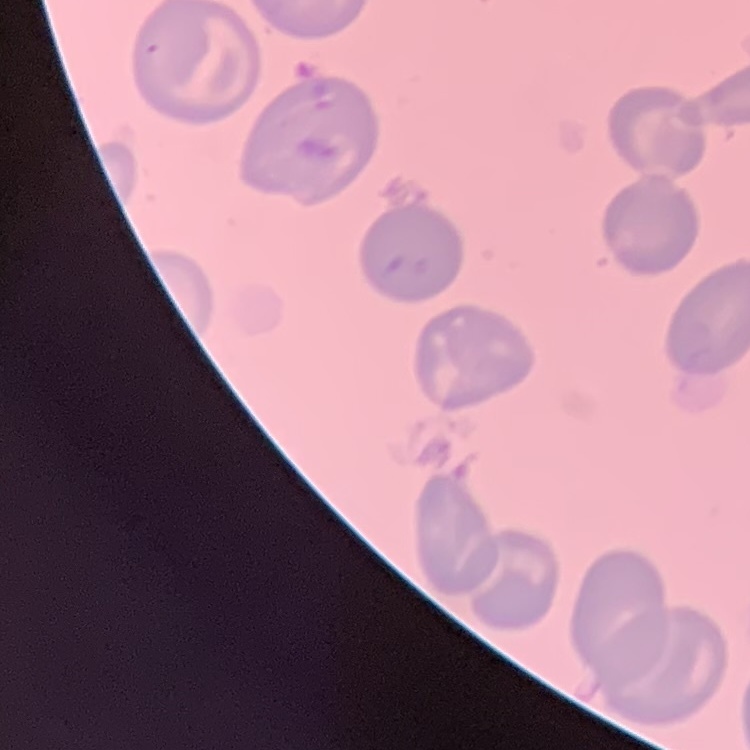

Summary:
  - Red blood cell morphology: no rouleaux formation
  - Image type: square crop of a larger photomicrograph
  - Stain: Field's or Giemsa
  - Preparation: thin blood film